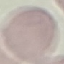

Malaria status: uninfected. Automatically extracted cell patch, resized to 64 × 64 pixels. Giemsa stain. Thin blood film. Acquired by smartphone through the microscope eyepiece.